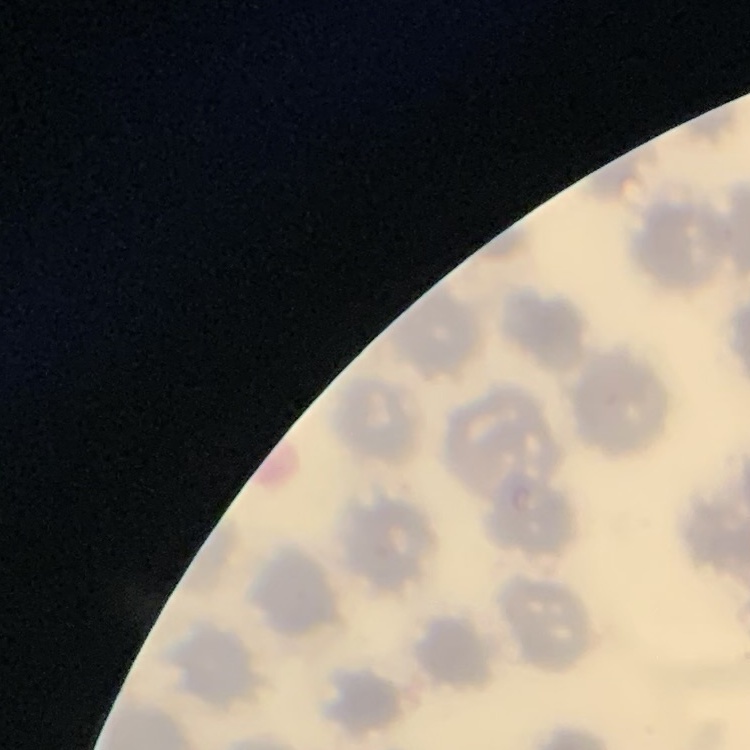

red blood cell morphology = no rouleaux formation
stain = Field's or Giemsa
image type = square crop of a larger photomicrograph
preparation = thin blood smear